Classify this cell by malaria status.
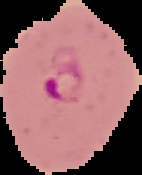
Parasitized.

image_size: 142×175 pixels
image_type: segmented cell region on a black background
preparation: thin blood smear